Outline each blood parasite and name the species.
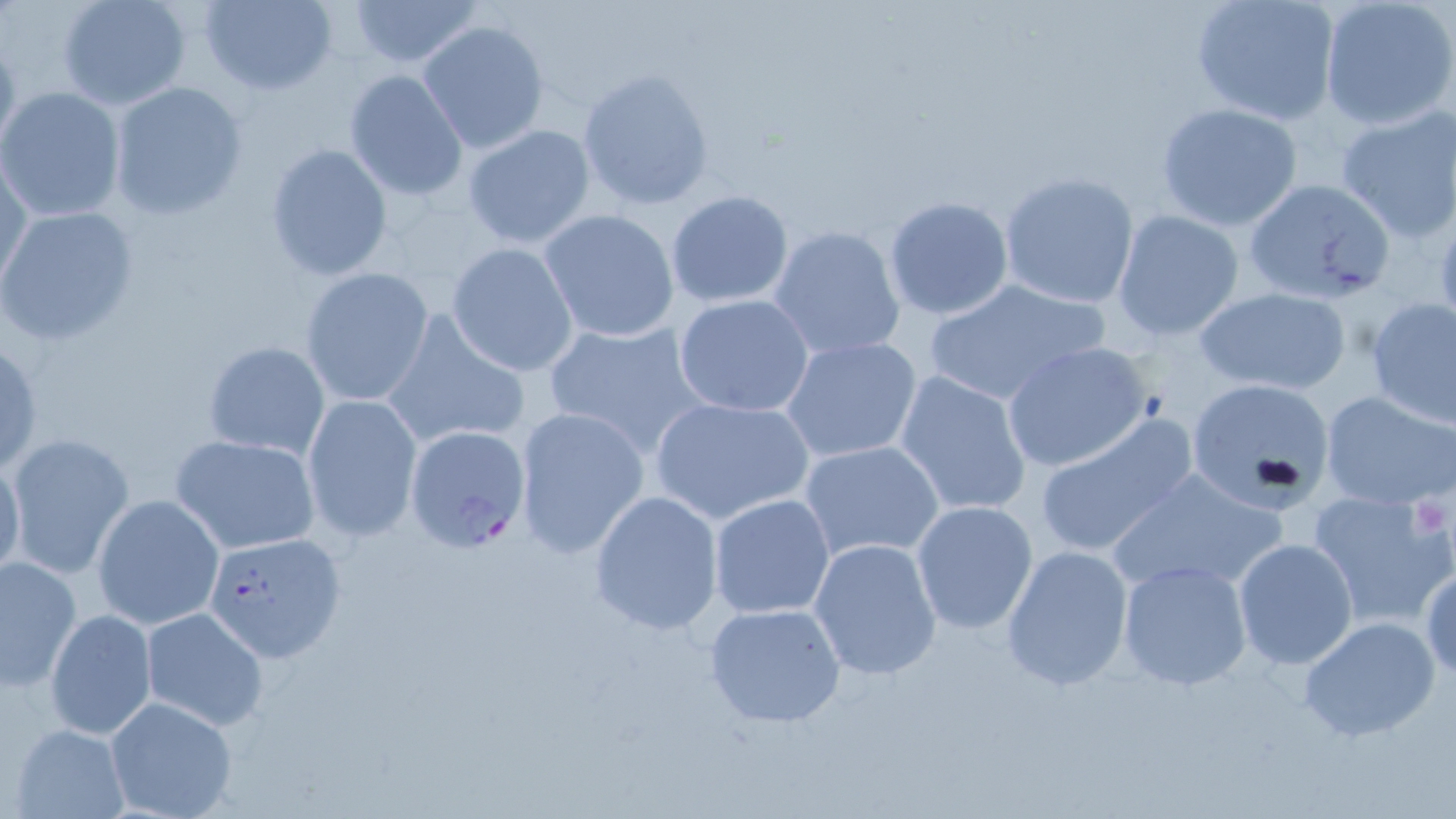
Approximate bounding boxes as [x1, y1, x2, y2] in pixels.
Plasmodium falciparum-infected red blood cells: [405, 426, 533, 555], [204, 532, 345, 660].
No Plasmodium ovale, Plasmodium malariae, Plasmodium vivax, Babesia divergens, or Trypanosoma brucei observed.

Uninfected red blood cell locations: [56, 0, 192, 110], [199, 0, 339, 97], [347, 0, 484, 67], [1190, 0, 1340, 126], [1319, 0, 1456, 131], [417, 19, 550, 154], [0, 33, 21, 160], [577, 67, 715, 210], [343, 70, 468, 201], [108, 81, 249, 220], [0, 87, 126, 223], [1156, 103, 1301, 231], [1334, 103, 1456, 242], [462, 123, 596, 248], [264, 142, 394, 282], [1, 150, 30, 292], [997, 171, 1140, 308], [1242, 177, 1396, 306], [665, 190, 794, 308], [883, 195, 1014, 321], [0, 204, 138, 345], [540, 208, 679, 342], [1113, 209, 1244, 341], [769, 225, 906, 361], [446, 242, 578, 377], [299, 267, 434, 407], [921, 276, 1110, 408], [1191, 286, 1353, 395], [674, 294, 814, 417], [1365, 296, 1455, 428], [383, 309, 531, 451], [540, 318, 712, 460], [778, 336, 925, 465], [0, 337, 44, 478], [1000, 340, 1154, 473], [201, 341, 330, 461], [894, 370, 1032, 518], [1185, 379, 1336, 508], [1321, 389, 1455, 512], [301, 392, 423, 542], [649, 394, 815, 525], [512, 404, 649, 560], [1033, 415, 1201, 559], [5, 433, 137, 579], [172, 434, 321, 554], [800, 440, 944, 563], [0, 450, 26, 589], [1108, 466, 1287, 596], [1306, 487, 1454, 629], [588, 491, 725, 635], [709, 493, 836, 620], [92, 494, 224, 629], [911, 501, 1038, 634], [808, 536, 943, 682], [1233, 538, 1361, 670], [999, 544, 1134, 692], [1, 554, 82, 692], [1116, 560, 1253, 691], [1421, 566, 1455, 679], [702, 602, 848, 729], [139, 607, 268, 730], [44, 608, 157, 741], [1299, 616, 1441, 742], [104, 696, 240, 819], [11, 723, 132, 817]. Platelet locations: [1408, 491, 1452, 534]. Slide-level diagnosis: Plasmodium falciparum. Thin blood film. May-Grünwald-Giemsa-stained preparation. One field of a larger specimen. Captured at 1000x magnification. Image is 1456×819 pixels. Optical microscopy.